Locate platelets.
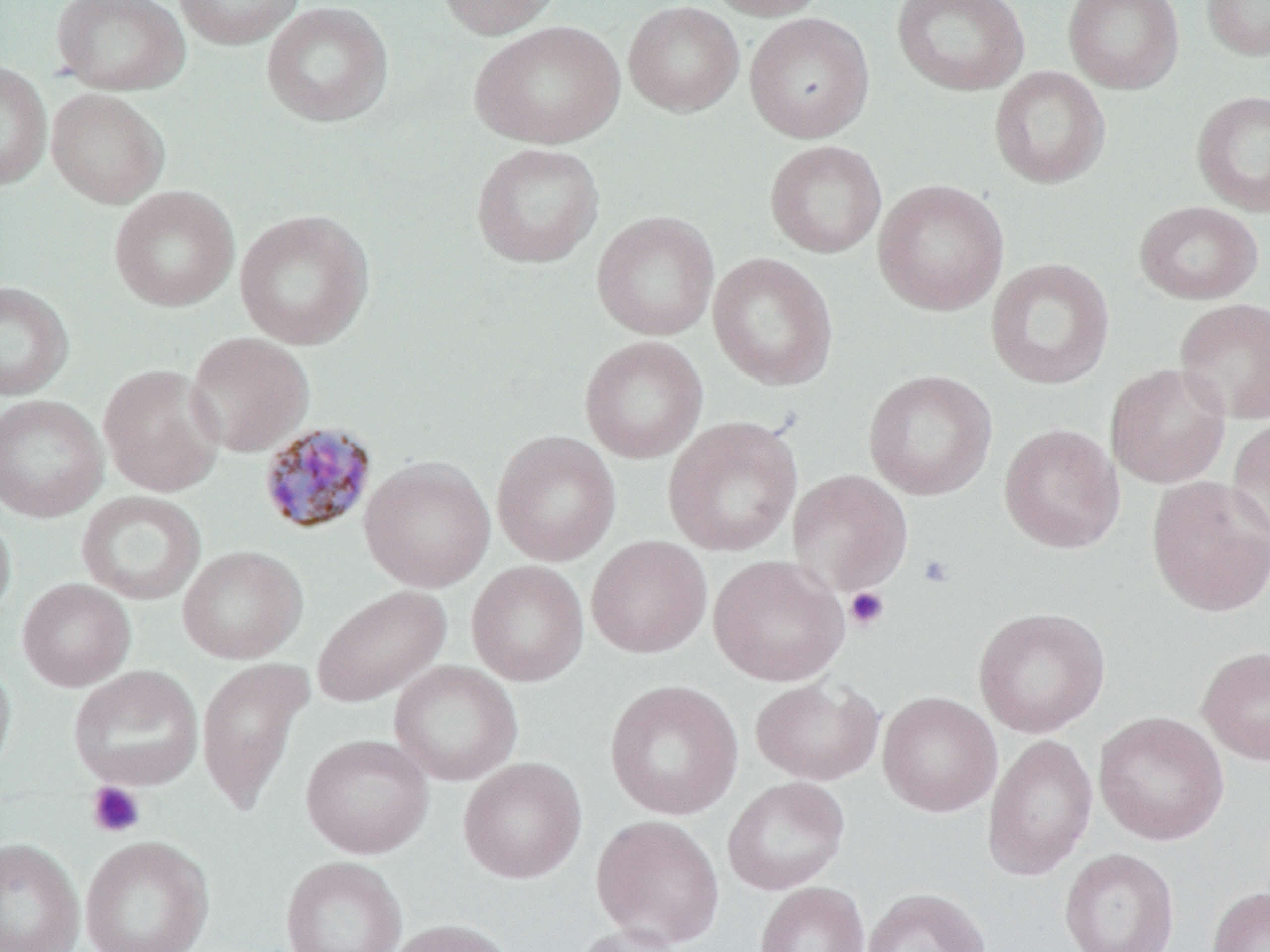

Approximate bounding boxes as named x1/y1/x2/y2 corners in pixels.
Platelets: (x1=917, y1=554, x2=955, y2=589), (x1=845, y1=587, x2=890, y2=632), (x1=87, y1=781, x2=146, y2=838).

Summary:
  - Uninfected red blood cell locations: (x1=50, y1=0, x2=190, y2=95), (x1=172, y1=0, x2=305, y2=50), (x1=435, y1=0, x2=563, y2=38), (x1=702, y1=0, x2=831, y2=20), (x1=889, y1=0, x2=1030, y2=96), (x1=1063, y1=0, x2=1184, y2=93), (x1=1201, y1=0, x2=1270, y2=61), (x1=261, y1=1, x2=394, y2=128), (x1=623, y1=1, x2=744, y2=116), (x1=744, y1=12, x2=875, y2=143), (x1=470, y1=19, x2=625, y2=149), (x1=0, y1=62, x2=51, y2=191), (x1=989, y1=66, x2=1110, y2=188), (x1=46, y1=88, x2=170, y2=208), (x1=1191, y1=90, x2=1270, y2=217), (x1=764, y1=140, x2=886, y2=258), (x1=471, y1=142, x2=605, y2=268), (x1=873, y1=179, x2=1009, y2=316), (x1=109, y1=186, x2=239, y2=312), (x1=1134, y1=200, x2=1263, y2=304), (x1=233, y1=208, x2=374, y2=350), (x1=592, y1=211, x2=720, y2=340), (x1=708, y1=253, x2=838, y2=390), (x1=985, y1=257, x2=1115, y2=390), (x1=0, y1=280, x2=73, y2=401), (x1=1174, y1=297, x2=1270, y2=424), (x1=186, y1=332, x2=314, y2=457), (x1=579, y1=335, x2=708, y2=463), (x1=1106, y1=363, x2=1231, y2=489), (x1=98, y1=364, x2=225, y2=496), (x1=863, y1=370, x2=997, y2=500), (x1=0, y1=393, x2=108, y2=523), (x1=1226, y1=415, x2=1270, y2=549), (x1=662, y1=416, x2=803, y2=557), (x1=999, y1=423, x2=1125, y2=554), (x1=492, y1=430, x2=621, y2=567), (x1=359, y1=456, x2=495, y2=592), (x1=787, y1=470, x2=914, y2=596), (x1=1146, y1=475, x2=1270, y2=617), (x1=76, y1=490, x2=206, y2=605), (x1=0, y1=507, x2=16, y2=629), (x1=586, y1=536, x2=712, y2=658), (x1=177, y1=545, x2=308, y2=664), (x1=708, y1=555, x2=848, y2=686), (x1=467, y1=561, x2=589, y2=686), (x1=17, y1=578, x2=136, y2=691), (x1=311, y1=585, x2=451, y2=708), (x1=973, y1=606, x2=1111, y2=737), (x1=1196, y1=645, x2=1270, y2=766), (x1=0, y1=650, x2=17, y2=788), (x1=195, y1=657, x2=312, y2=816), (x1=389, y1=661, x2=523, y2=786), (x1=69, y1=665, x2=204, y2=791), (x1=750, y1=678, x2=884, y2=786), (x1=604, y1=679, x2=743, y2=820), (x1=878, y1=691, x2=1002, y2=817), (x1=1094, y1=711, x2=1229, y2=845), (x1=983, y1=732, x2=1098, y2=881), (x1=300, y1=733, x2=433, y2=858), (x1=458, y1=757, x2=587, y2=883), (x1=722, y1=776, x2=850, y2=895), (x1=590, y1=814, x2=725, y2=948), (x1=80, y1=835, x2=214, y2=952), (x1=0, y1=837, x2=85, y2=952), (x1=1058, y1=847, x2=1179, y2=952), (x1=280, y1=855, x2=407, y2=952), (x1=755, y1=882, x2=869, y2=952), (x1=1207, y1=886, x2=1270, y2=952), (x1=861, y1=888, x2=991, y2=952), (x1=384, y1=918, x2=516, y2=952), (x1=571, y1=922, x2=687, y2=952)
  - Plasmodium malariae-infected red blood cell locations: (x1=257, y1=421, x2=378, y2=536)
  - Slide-level diagnosis: Plasmodium malariae
  - Modality: optical microscopy
  - Field of view: one of a larger specimen
  - Image size: 1270×952 pixels
  - Preparation: thin blood film
  - Magnification: 1000x
  - Stain: May-Grünwald-Giemsa